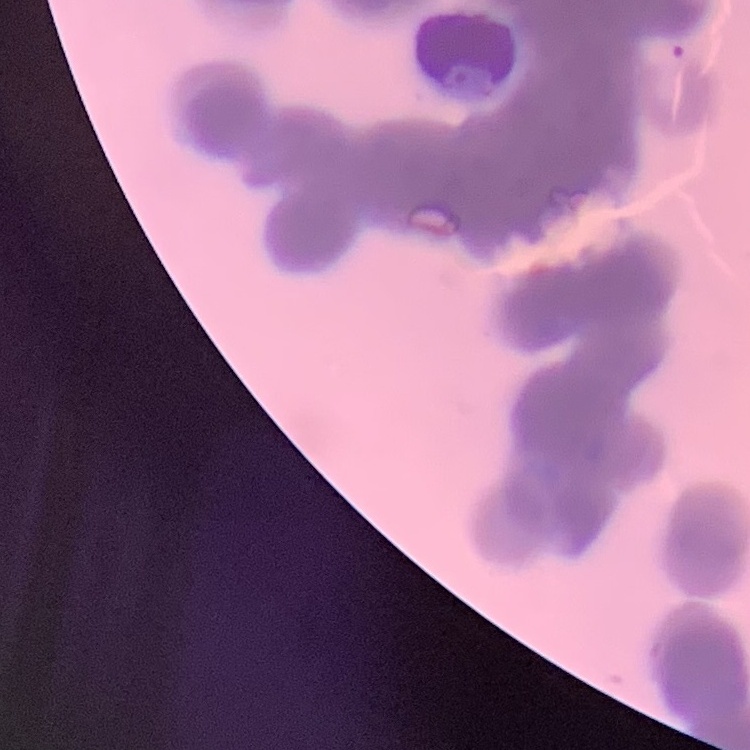

Summary:
  - Erythrocyte morphology: rouleaux formation
  - Image type: one tile cut from a larger photomicrograph
  - Preparation: thin blood smear
  - Stain: Field's or Giemsa